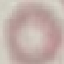
malaria_status: uninfected
preparation: thin blood film
capture: smartphone through the microscope eyepiece
stain: Giemsa
image_type: cell patch, automatically extracted from a larger field of view and resized to 64 × 64 pixels